Outline each Plasmodium falciparum-infected red blood cell.
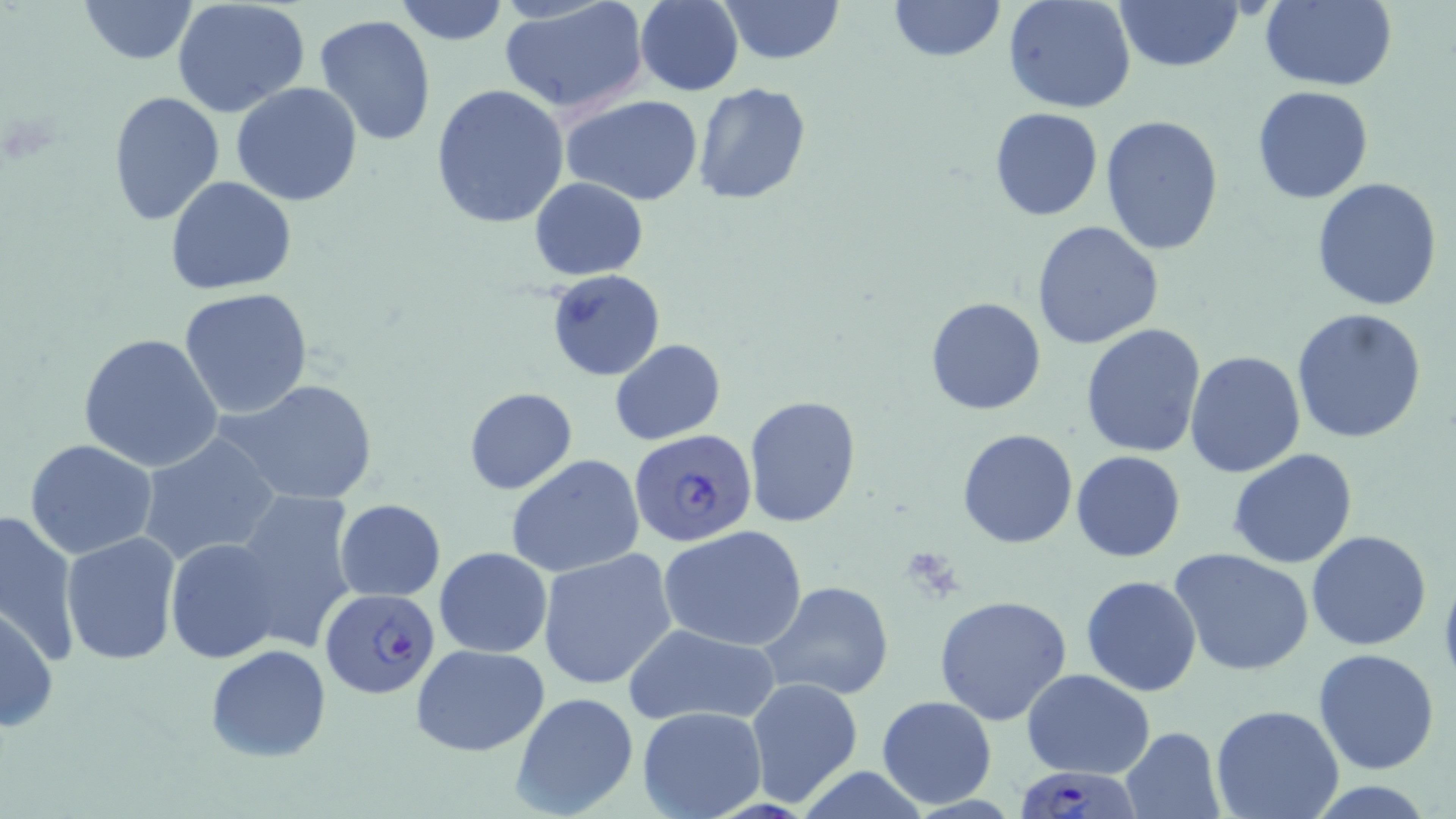
Approximate bounding boxes as named x1/y1/x2/y2 corners in pixels.
Plasmodium falciparum-infected red blood cells: (x1=629, y1=428, x2=760, y2=549), (x1=319, y1=591, x2=440, y2=702), (x1=1020, y1=770, x2=1137, y2=819).

slide-level diagnosis = Plasmodium falciparum
field of view = single
modality = light microscopy
uninfected red blood cell locations = approximate bounding boxes as named x1/y1/x2/y2 corners in pixels: (x1=79, y1=0, x2=198, y2=65), (x1=172, y1=0, x2=310, y2=115), (x1=393, y1=0, x2=509, y2=46), (x1=499, y1=0, x2=649, y2=117), (x1=717, y1=0, x2=844, y2=65), (x1=888, y1=0, x2=1003, y2=61), (x1=1115, y1=0, x2=1243, y2=71), (x1=1259, y1=0, x2=1397, y2=90), (x1=634, y1=1, x2=743, y2=96), (x1=1005, y1=1, x2=1136, y2=114), (x1=312, y1=13, x2=438, y2=146), (x1=692, y1=82, x2=812, y2=206), (x1=231, y1=83, x2=364, y2=205), (x1=429, y1=85, x2=571, y2=230), (x1=1252, y1=85, x2=1374, y2=204), (x1=108, y1=90, x2=225, y2=224), (x1=559, y1=94, x2=705, y2=205), (x1=989, y1=107, x2=1103, y2=220), (x1=1099, y1=115, x2=1224, y2=257), (x1=165, y1=175, x2=297, y2=295), (x1=1311, y1=175, x2=1444, y2=310), (x1=530, y1=177, x2=648, y2=280), (x1=1031, y1=221, x2=1164, y2=352), (x1=546, y1=269, x2=664, y2=382), (x1=178, y1=287, x2=313, y2=418), (x1=926, y1=297, x2=1046, y2=416), (x1=1291, y1=309, x2=1430, y2=446), (x1=1080, y1=324, x2=1207, y2=458), (x1=77, y1=332, x2=224, y2=473), (x1=609, y1=339, x2=725, y2=445), (x1=1186, y1=351, x2=1306, y2=478), (x1=225, y1=379, x2=379, y2=505), (x1=465, y1=387, x2=577, y2=494), (x1=743, y1=394, x2=862, y2=528), (x1=956, y1=428, x2=1078, y2=549), (x1=137, y1=431, x2=280, y2=567), (x1=25, y1=439, x2=159, y2=560), (x1=1228, y1=448, x2=1359, y2=569), (x1=1072, y1=450, x2=1185, y2=561), (x1=506, y1=455, x2=645, y2=578), (x1=231, y1=491, x2=360, y2=648), (x1=333, y1=499, x2=446, y2=601), (x1=0, y1=506, x2=81, y2=667), (x1=660, y1=525, x2=808, y2=651), (x1=1306, y1=529, x2=1432, y2=650), (x1=61, y1=531, x2=181, y2=665), (x1=163, y1=536, x2=284, y2=665), (x1=433, y1=546, x2=552, y2=658), (x1=538, y1=549, x2=681, y2=691), (x1=1170, y1=549, x2=1316, y2=678), (x1=1081, y1=574, x2=1202, y2=697), (x1=760, y1=579, x2=895, y2=701), (x1=933, y1=595, x2=1073, y2=725), (x1=0, y1=603, x2=57, y2=735), (x1=623, y1=622, x2=781, y2=728), (x1=410, y1=642, x2=549, y2=756), (x1=205, y1=643, x2=332, y2=761), (x1=1313, y1=648, x2=1441, y2=775), (x1=1022, y1=669, x2=1155, y2=778), (x1=745, y1=677, x2=864, y2=807), (x1=1227, y1=682, x2=1429, y2=804), (x1=510, y1=692, x2=637, y2=817), (x1=876, y1=694, x2=998, y2=808), (x1=636, y1=705, x2=767, y2=819), (x1=1211, y1=705, x2=1344, y2=819), (x1=1121, y1=727, x2=1225, y2=818), (x1=1302, y1=781, x2=1444, y2=817)
image size = 1456×819 pixels
preparation = thin blood smear
magnification = 1000x
stain = May-Grünwald-Giemsa